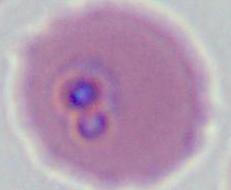
A Plasmodium parasite is seen. 400x or 1000x magnification. Micrograph.